State which parasite is depicted.
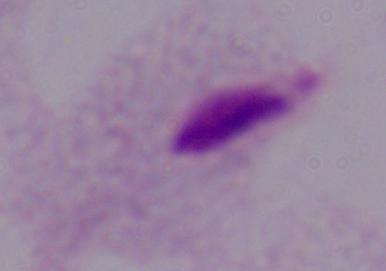

A trichomonad.

Micrograph. 1000x magnification.